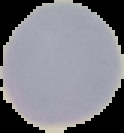
image_type: cell region segmented out of the field of view; surrounding area masked to black
preparation: thin blood film
image_size: 124×133 pixels
malaria_status: uninfected